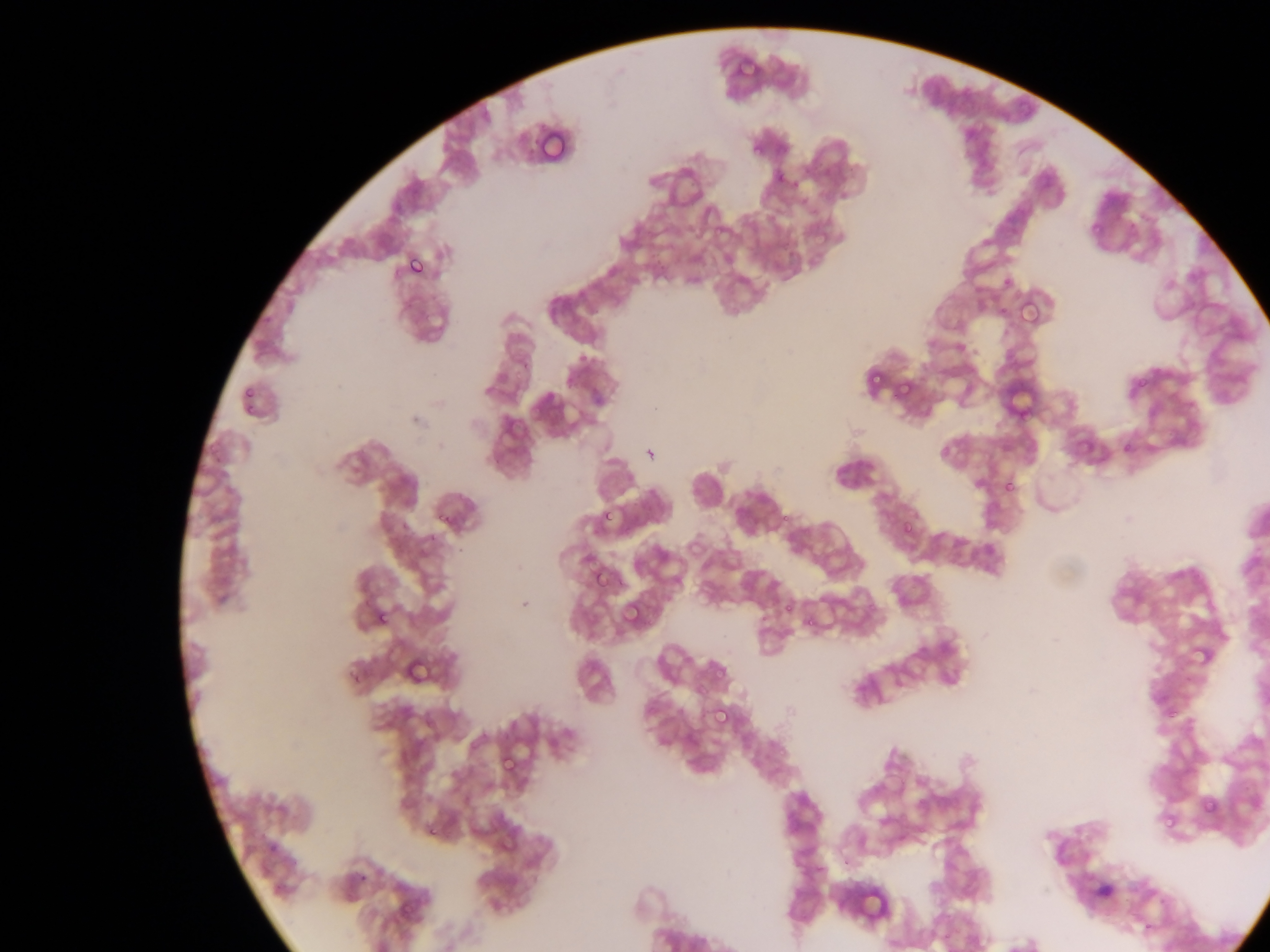

Approximate bounding boxes as {left, top, right, bottom} in pixels.
Summary:
  - Plasmodium parasite locations: {536, 123, 570, 155}, {751, 142, 766, 157}, {772, 175, 790, 189}, {1087, 217, 1108, 235}, {404, 251, 430, 281}, {1015, 297, 1043, 329}, {865, 370, 884, 388}, {896, 374, 914, 399}, {1000, 478, 1019, 498}, {434, 504, 454, 525}, {602, 507, 617, 525}, {897, 515, 923, 543}, {900, 521, 917, 539}, {588, 566, 611, 592}, {619, 599, 647, 628}, {373, 607, 393, 629}, {1187, 644, 1210, 667}, {402, 647, 445, 690}, {710, 703, 734, 730}, {497, 751, 522, 779}, {1201, 799, 1222, 818}, {1159, 816, 1172, 829}, {425, 821, 448, 841}, {855, 887, 892, 910}
  - Capture: mobile-phone photograph through a microscope
  - Country: Ghana
  - Field of view: single
  - Image size: 1270×952 pixels
  - Preparation: thin blood film